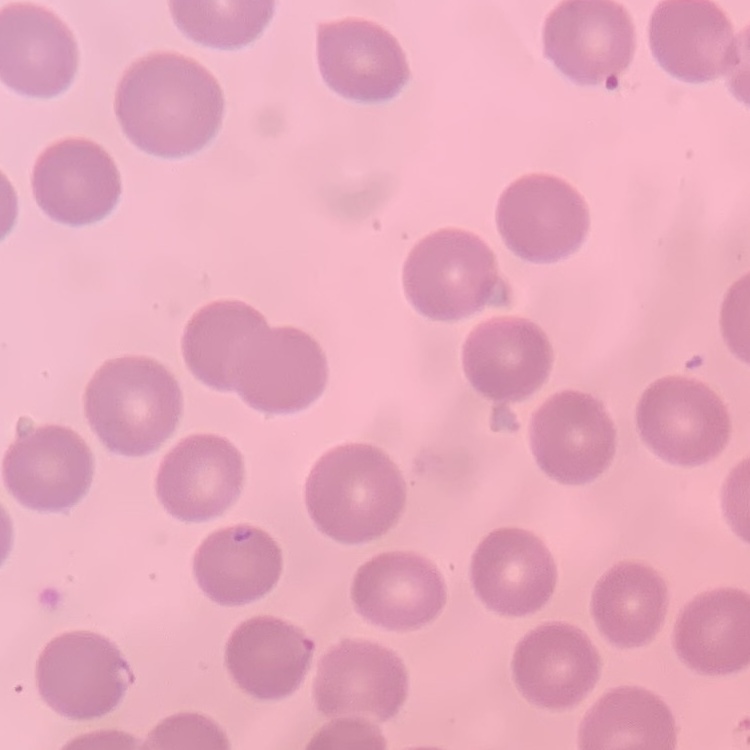

erythrocyte morphology = no rouleaux formation
image type = one tile cut from a larger photomicrograph
stain = Field's or Giemsa
preparation = thin peripheral smear